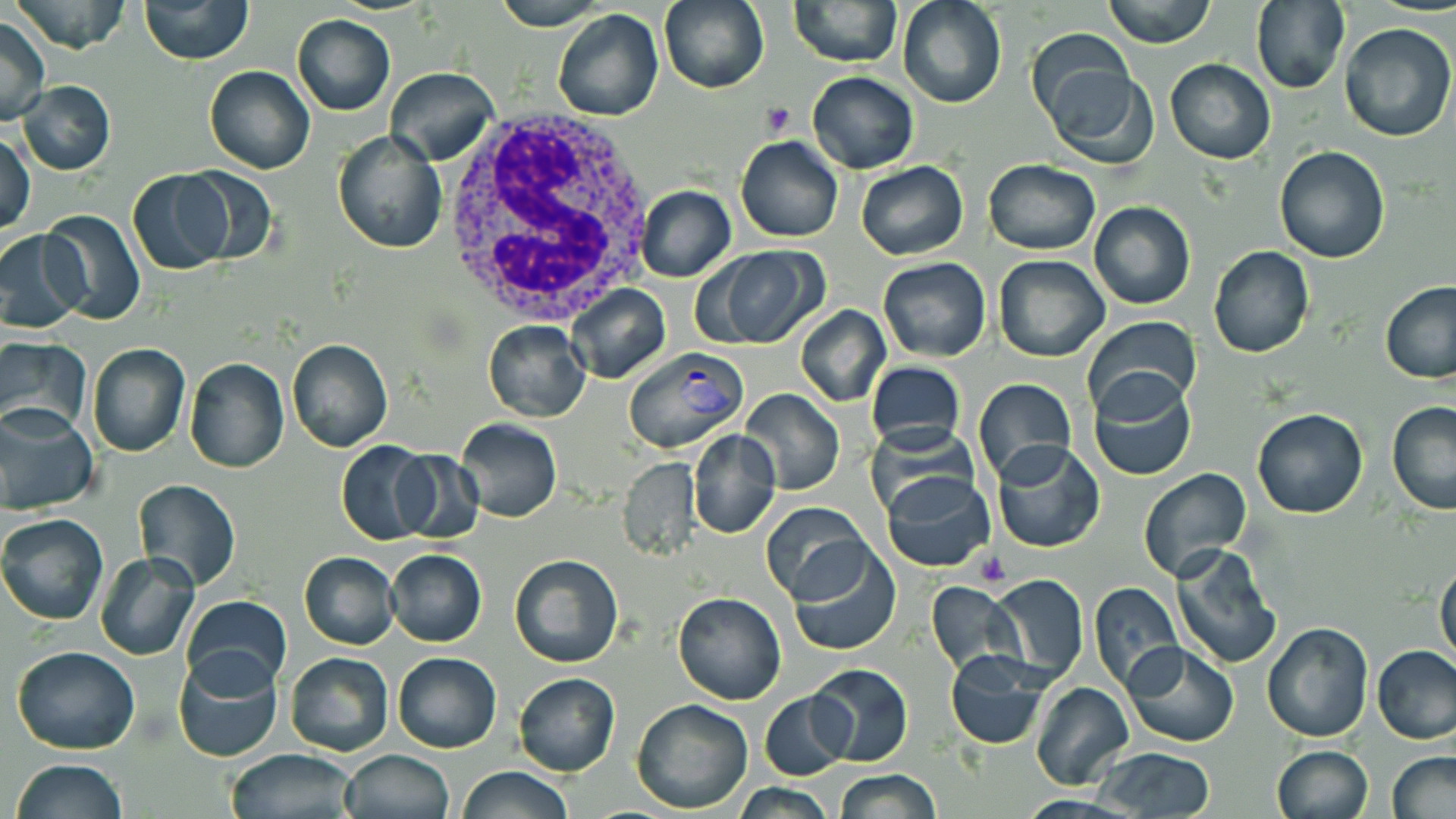

slide_level_diagnosis: Plasmodium vivax
field_of_view: single
plasmodium_vivax_infected_red_blood_cell_locations: 'approximate bounding boxes as [x1, y1, x2, y2] in pixels: [622, 345, 749, 454]'
stain: May-Grünwald-Giemsa
preparation: thin blood film
modality: optical microscopy
image_size: 1456×819 pixels
uninfected_red_blood_cell_locations: 'approximate bounding boxes as [x1, y1, x2, y2] in pixels: [13, 0, 130, 52], [139, 0, 253, 64], [491, 0, 612, 29], [659, 0, 768, 93], [789, 0, 902, 68], [898, 0, 1006, 108], [1103, 0, 1218, 48], [1249, 0, 1351, 96], [552, 8, 664, 122], [293, 13, 396, 115], [0, 15, 49, 125], [1339, 21, 1455, 142], [1023, 30, 1137, 134], [1165, 59, 1277, 165], [204, 65, 315, 175], [1041, 66, 1158, 168], [385, 67, 500, 166], [806, 72, 919, 174], [18, 80, 116, 174], [1, 130, 36, 234], [333, 131, 446, 253], [734, 136, 843, 242], [1273, 146, 1393, 263], [983, 159, 1100, 256], [856, 160, 968, 260], [177, 166, 277, 267], [128, 170, 232, 274], [636, 184, 737, 282], [1089, 201, 1196, 310], [41, 210, 147, 325], [0, 231, 87, 334], [1208, 246, 1315, 361], [697, 248, 827, 350], [993, 254, 1109, 362], [878, 256, 990, 362], [1379, 281, 1456, 384], [565, 284, 671, 382], [794, 305, 890, 406], [1080, 316, 1200, 422], [482, 319, 592, 423], [0, 338, 92, 437], [286, 339, 392, 452], [86, 344, 190, 458], [183, 356, 290, 472], [866, 361, 965, 454], [1086, 373, 1198, 483], [973, 378, 1076, 487], [740, 389, 845, 494], [1387, 401, 1456, 515], [0, 406, 99, 515], [1252, 408, 1368, 519], [454, 419, 561, 522], [688, 429, 782, 539], [335, 442, 436, 543], [993, 442, 1107, 553], [392, 451, 485, 544], [616, 457, 702, 562], [1137, 466, 1253, 582], [880, 469, 995, 571], [132, 479, 239, 591], [760, 504, 872, 605], [0, 513, 108, 624], [788, 540, 903, 658], [1168, 543, 1282, 670], [384, 548, 487, 647], [299, 551, 401, 649], [95, 554, 199, 661], [509, 554, 623, 669], [1434, 559, 1456, 670], [985, 573, 1090, 684], [925, 582, 1021, 676], [1089, 582, 1187, 693], [672, 592, 786, 705], [181, 597, 291, 694], [1262, 622, 1374, 741], [1123, 642, 1240, 748], [1370, 644, 1456, 747], [11, 645, 140, 755], [945, 649, 1054, 749], [172, 650, 283, 763], [284, 651, 394, 757], [393, 652, 502, 753], [806, 662, 913, 767], [513, 673, 620, 777], [1029, 681, 1135, 791], [758, 692, 853, 779], [631, 698, 752, 813], [1271, 745, 1374, 819], [1092, 747, 1216, 818], [224, 750, 362, 819], [341, 750, 454, 819], [1386, 750, 1456, 819], [11, 758, 128, 818], [456, 766, 573, 819], [834, 768, 942, 818], [733, 782, 836, 818]'
white_blood_cell_locations: 'approximate bounding boxes as [x1, y1, x2, y2] in pixels: [433, 111, 659, 329]'
platelet_locations: 'approximate bounding boxes as [x1, y1, x2, y2] in pixels: [761, 101, 796, 139], [974, 550, 1010, 588]'
magnification: 1000x